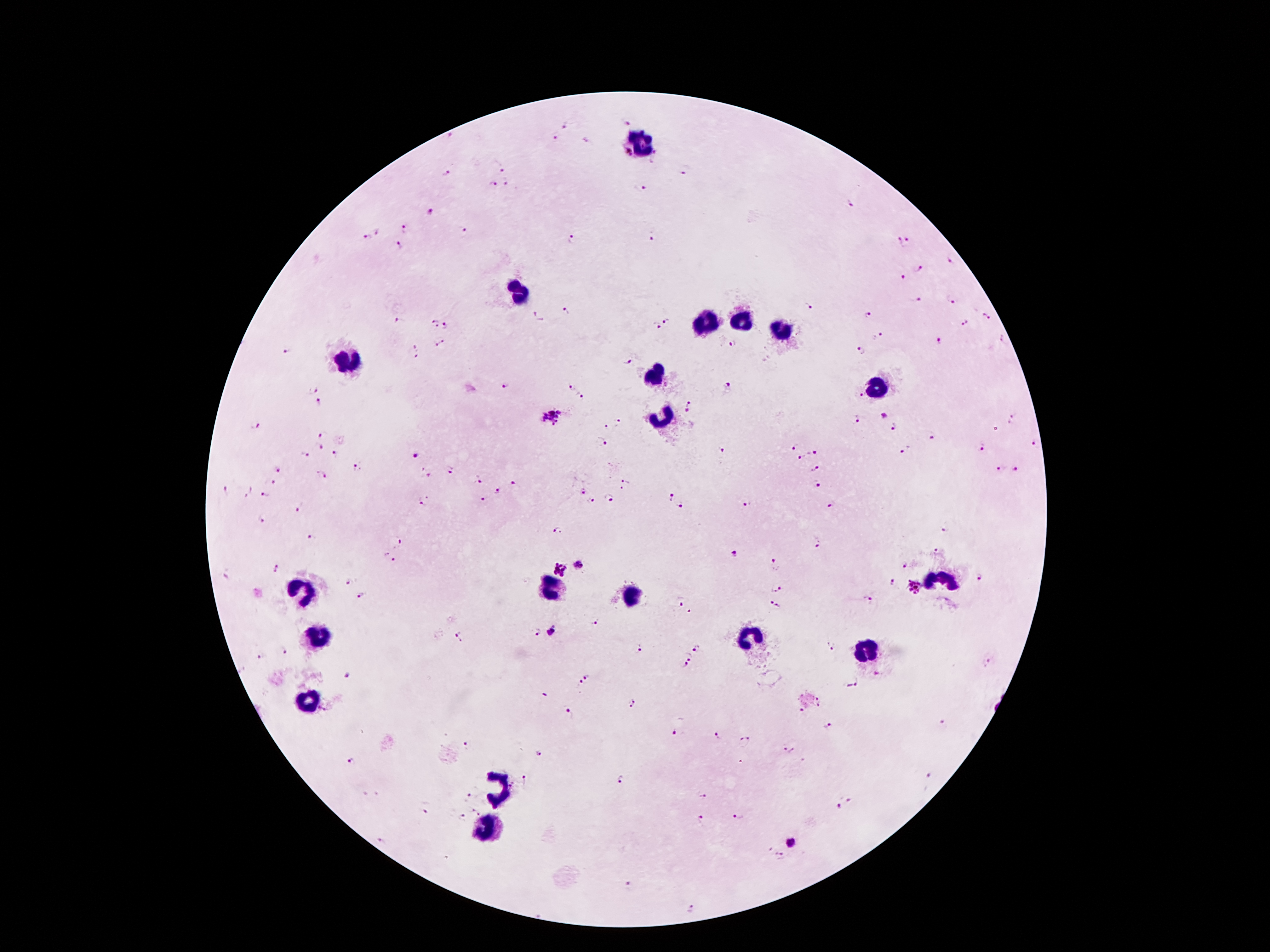

coordinate format = approximate centers as [x, y] in pixels
malaria parasite locations = [623, 123], [566, 125], [449, 136], [556, 138], [629, 153], [657, 154], [502, 168], [685, 170], [447, 176], [507, 182], [493, 185], [640, 190], [848, 203], [431, 212], [465, 228], [379, 230], [405, 230], [367, 237], [651, 237], [908, 238], [572, 240], [899, 242], [399, 246], [951, 260], [919, 268], [903, 278], [952, 300], [916, 302], [808, 307], [566, 311], [867, 314], [987, 316], [538, 318], [667, 320], [400, 322], [964, 323], [434, 326], [447, 326], [656, 326], [878, 336], [1003, 338], [939, 341], [442, 342], [734, 344], [417, 348], [287, 351], [861, 352], [417, 356], [628, 362], [506, 386], [572, 386], [729, 387], [313, 390], [861, 393], [583, 397], [321, 402], [689, 406], [884, 415], [553, 417], [1012, 418], [618, 420], [855, 420], [255, 427], [605, 427], [894, 427], [324, 436], [931, 437], [602, 441], [1034, 442], [319, 446], [983, 448], [792, 449], [904, 449], [723, 450], [813, 452], [303, 453], [338, 455], [417, 455], [803, 458], [815, 466], [358, 467], [279, 469], [1001, 469], [452, 470], [1016, 470], [426, 473], [321, 474], [624, 479], [477, 481], [271, 482], [817, 484], [516, 485], [621, 489], [226, 491], [247, 491], [500, 492], [582, 492], [263, 495], [671, 496], [609, 497], [484, 499], [591, 501], [425, 502], [681, 502], [747, 505], [831, 505], [298, 507], [265, 520], [945, 528], [557, 531], [312, 538], [396, 541], [818, 544], [934, 549], [735, 553], [390, 559], [775, 562], [903, 564], [578, 565], [275, 567], [559, 569], [226, 576], [981, 576], [351, 583], [892, 583], [915, 587], [776, 588], [363, 595], [870, 599], [678, 601], [775, 604], [690, 611], [595, 622], [552, 631], [535, 632], [460, 637], [831, 647], [698, 648], [637, 649], [283, 651], [261, 658], [689, 658], [684, 665], [346, 675], [588, 676], [854, 683], [579, 684], [821, 702], [633, 703], [322, 709], [799, 711], [570, 715], [942, 723], [830, 726], [676, 733], [717, 736], [744, 742], [466, 745], [789, 750], [539, 753], [351, 761], [928, 774], [621, 779], [526, 781], [469, 796], [703, 797], [849, 803], [837, 807], [426, 808], [475, 813], [739, 815], [463, 818], [700, 820], [381, 842], [792, 842], [780, 856], [630, 885], [693, 909]
leukocyte locations = [639, 140], [520, 292], [739, 322], [703, 325], [780, 328], [348, 360], [654, 377], [877, 389], [664, 419], [940, 578], [551, 589], [300, 593], [631, 596], [321, 635], [746, 639], [864, 650], [309, 700], [500, 788], [489, 829]
patient malaria status = positive for Plasmodium falciparum
magnification = 100x
field of view = single
image size = 1270×952 pixels
stain = Giemsa
capture = smartphone through the microscope eyepiece
preparation = thick blood smear